State which parasite is depicted.
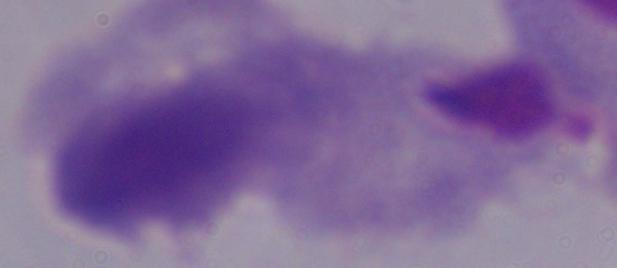
A trichomonad.

{
  "magnification": "1000x",
  "modality": "photomicrograph"
}